Report the malaria status of this cell.
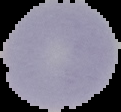
Uninfected.

From a thin blood film. Image is 121×112 pixels. Segmented cell region on a black background.